Comment on the morphology of the erythrocytes.
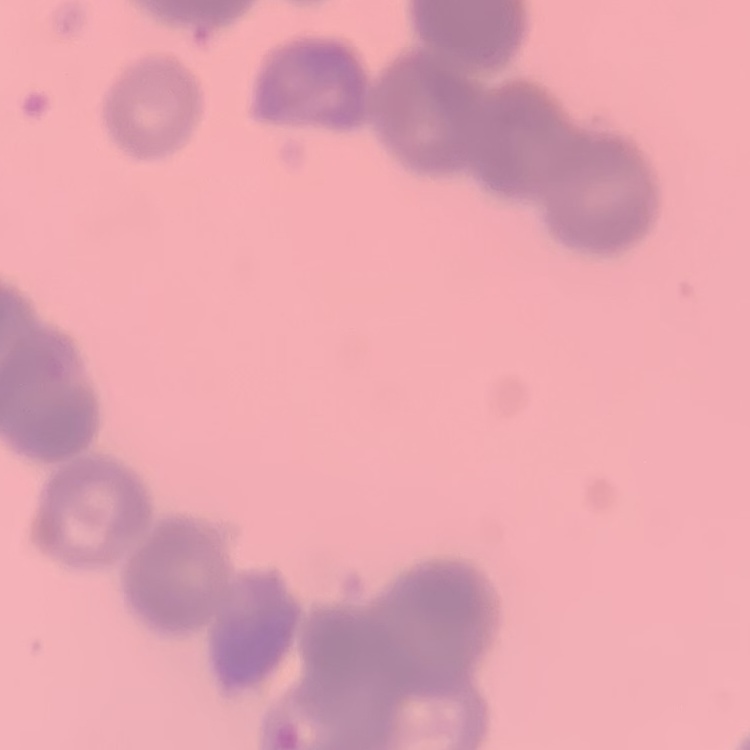
Rouleaux formation.

Summary:
  - Image type: square crop of a larger photomicrograph
  - Preparation: thin blood film
  - Stain: Field's or Giemsa